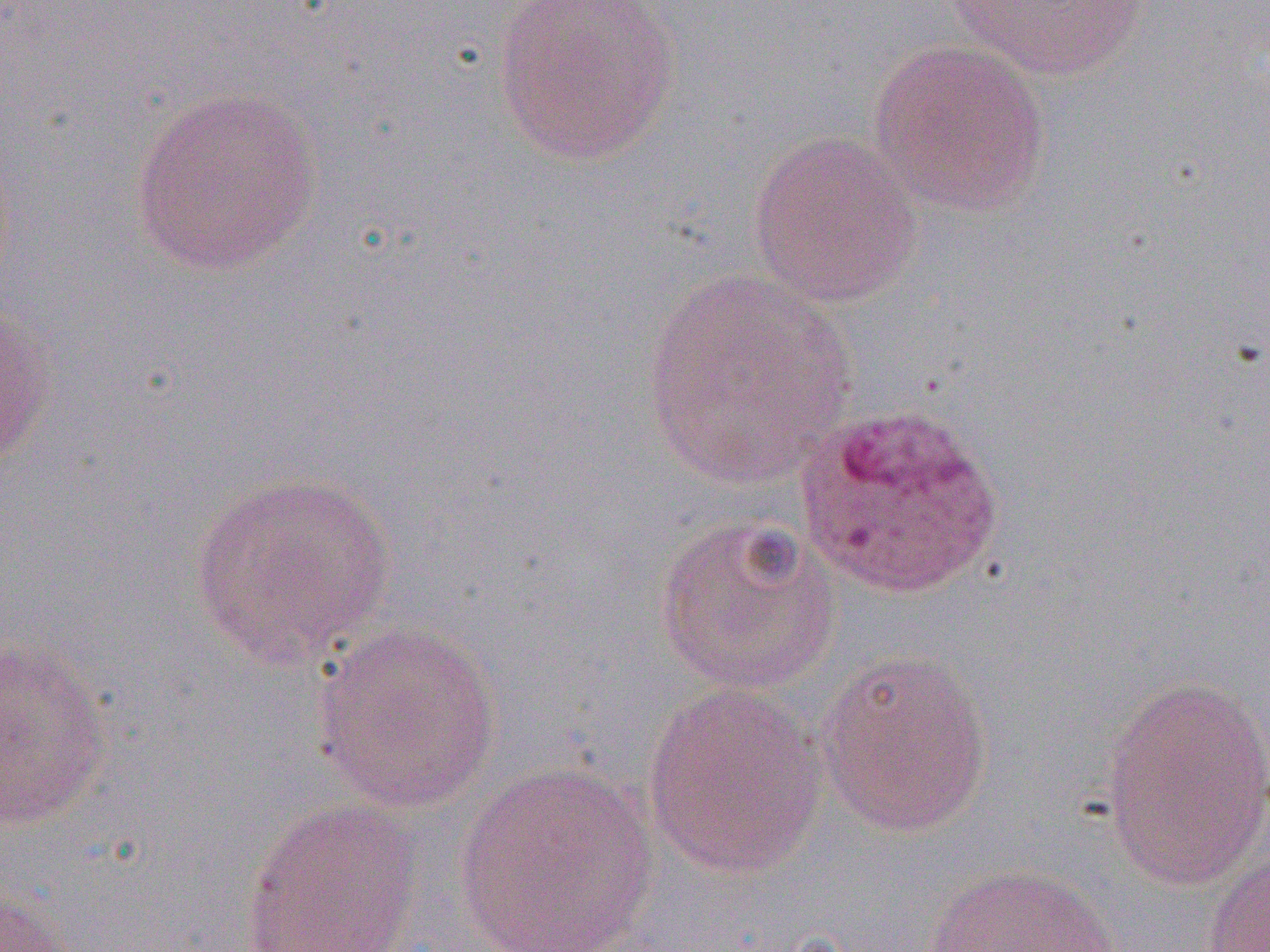 Approximate bounding boxes as named x1/y1/x2/y2 corners in pixels. Plasmodium ovale-infected red blood cell locations: (x1=794, y1=402, x2=1005, y2=601). Uninfected red blood cell locations: (x1=489, y1=0, x2=683, y2=169), (x1=943, y1=0, x2=1150, y2=81), (x1=868, y1=39, x2=1051, y2=216), (x1=130, y1=84, x2=325, y2=279), (x1=747, y1=130, x2=923, y2=309), (x1=642, y1=268, x2=857, y2=489), (x1=0, y1=293, x2=56, y2=467), (x1=189, y1=469, x2=398, y2=669), (x1=653, y1=512, x2=843, y2=697), (x1=312, y1=620, x2=503, y2=813), (x1=0, y1=636, x2=114, y2=832), (x1=815, y1=648, x2=994, y2=839), (x1=1099, y1=674, x2=1270, y2=887), (x1=642, y1=682, x2=828, y2=880), (x1=453, y1=762, x2=660, y2=951), (x1=238, y1=798, x2=425, y2=952), (x1=1202, y1=846, x2=1270, y2=952), (x1=922, y1=863, x2=1121, y2=952), (x1=0, y1=887, x2=80, y2=952). Slide-level diagnosis: Plasmodium ovale. 1000x magnification. One field of a larger specimen. Optical microscopy. Thin blood smear. Image is 1270×952 pixels.